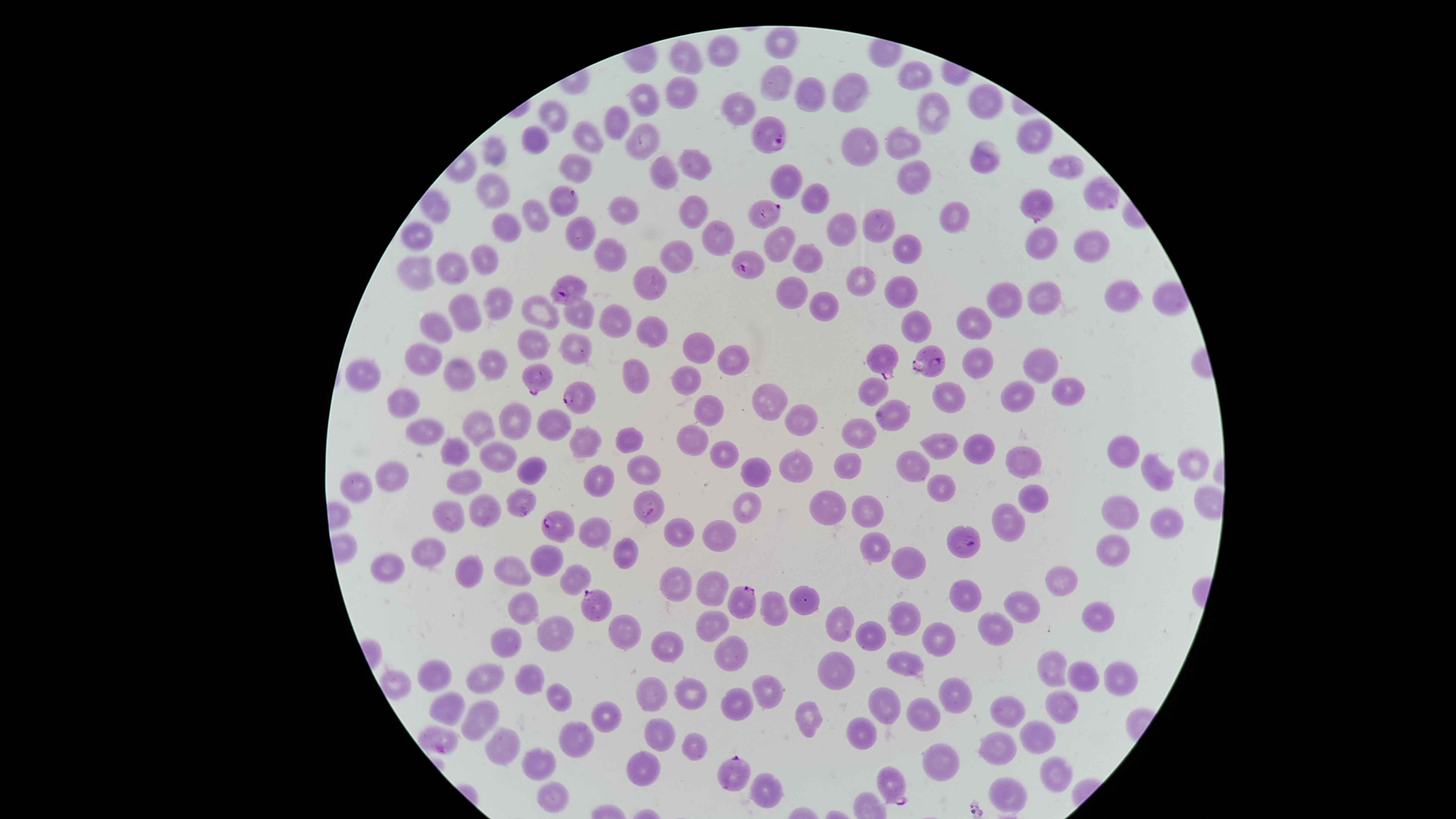

Approximate marker points as {x, y} in pixels.
Summary:
  - Parasitized RBCs: {770, 136}, {1100, 191}, {566, 198}, {1038, 205}, {767, 210}, {751, 268}, {571, 291}, {886, 359}, {935, 362}, {535, 375}, {577, 394}, {651, 507}, {564, 525}, {963, 542}, {745, 601}, {594, 606}, {433, 741}, {731, 773}, {891, 788}
  - Uninfected RBCs: {783, 45}, {721, 51}, {685, 56}, {913, 73}, {779, 76}, {678, 90}, {851, 93}, {803, 94}, {650, 100}, {986, 104}, {739, 115}, {550, 120}, {934, 120}, {622, 121}, {1032, 136}, {585, 138}, {645, 138}, {899, 139}, {538, 145}, {861, 145}, {498, 154}, {696, 161}, {985, 162}, {572, 164}, {1064, 167}, {664, 172}, {908, 172}, {786, 179}, {494, 189}, {812, 194}, {689, 208}, {435, 209}, {624, 209}, {532, 211}, {956, 215}, {880, 221}, {504, 228}, {844, 228}, {419, 233}, {721, 235}, {776, 235}, {911, 245}, {614, 248}, {1046, 248}, {1094, 248}, {674, 251}, {805, 256}, {483, 263}, {454, 268}, {418, 270}, {649, 274}, {863, 276}, {899, 289}, {1118, 290}, {793, 291}, {1003, 298}, {1033, 298}, {1166, 298}, {494, 302}, {821, 305}, {464, 311}, {543, 313}, {581, 320}, {616, 322}, {913, 324}, {971, 324}, {438, 331}, {649, 334}, {537, 345}, {691, 349}, {574, 352}, {426, 356}, {489, 360}, {728, 363}, {978, 365}, {1043, 369}, {457, 371}, {638, 374}, {365, 378}, {682, 382}, {873, 386}, {1072, 392}, {952, 395}, {766, 398}, {1016, 400}, {404, 403}, {708, 407}, {797, 413}, {893, 415}, {514, 416}, {551, 425}, {471, 428}, {862, 431}, {426, 436}, {692, 438}, {585, 442}, {942, 442}, {626, 443}, {973, 446}, {498, 451}, {457, 452}, {722, 452}, {1123, 452}, {786, 461}, {910, 461}, {1015, 461}, {850, 462}, {528, 463}, {642, 465}, {1193, 465}, {749, 468}, {1152, 472}, {392, 474}, {597, 478}, {356, 480}, {471, 483}, {941, 485}, {1034, 495}, {520, 501}, {830, 504}, {487, 509}, {742, 509}, {866, 509}, {1121, 509}, {454, 514}, {1164, 518}, {1012, 519}, {595, 533}, {724, 533}, {677, 538}, {876, 548}, {1114, 550}, {620, 552}, {428, 554}, {548, 560}, {394, 565}, {512, 566}, {910, 566}, {468, 568}, {580, 573}, {1066, 579}, {713, 584}, {683, 586}, {969, 592}, {804, 602}, {1022, 602}, {525, 606}, {777, 608}, {1096, 612}, {906, 617}, {713, 618}, {841, 620}, {552, 627}, {999, 627}, {627, 630}, {864, 630}, {935, 638}, {509, 642}, {667, 645}, {739, 653}, {833, 665}, {902, 665}, {1054, 667}, {434, 674}, {1085, 674}, {486, 676}, {536, 676}, {1119, 676}, {398, 681}, {768, 685}, {960, 689}, {693, 692}, {649, 694}, {560, 697}, {737, 703}, {1060, 704}, {891, 705}, {1011, 706}, {443, 710}, {808, 711}, {920, 712}, {607, 716}, {483, 717}, {862, 725}, {1038, 732}, {660, 735}, {508, 742}, {577, 742}, {697, 742}, {1001, 743}, {949, 759}, {643, 764}, {536, 768}, {1055, 770}, {768, 789}, {1011, 790}, {555, 801}
  - Field of view: single
  - Capture: smartphone photograph through the microscope eyepiece
  - Preparation: thin smear of blood
  - Image size: 1456×819 pixels
  - Species: Plasmodium falciparum
  - Stain: Giemsa
  - Presence: malaria parasites identified
  - Visible region: circular